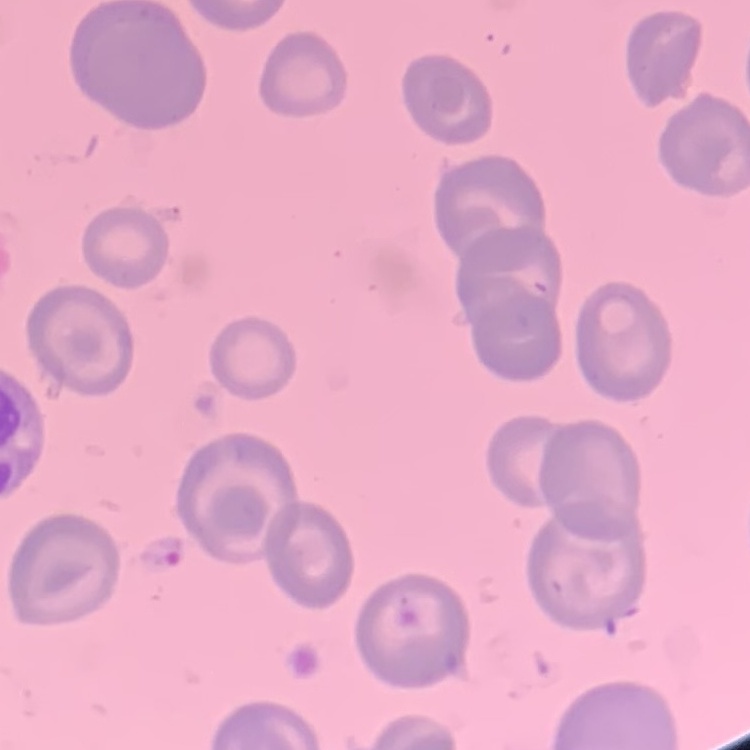 The red blood cells exhibit no rouleaux formation. Thin peripheral smear. One tile cut from a larger photomicrograph. Field's or Giemsa stain.